State the blood parasite species.
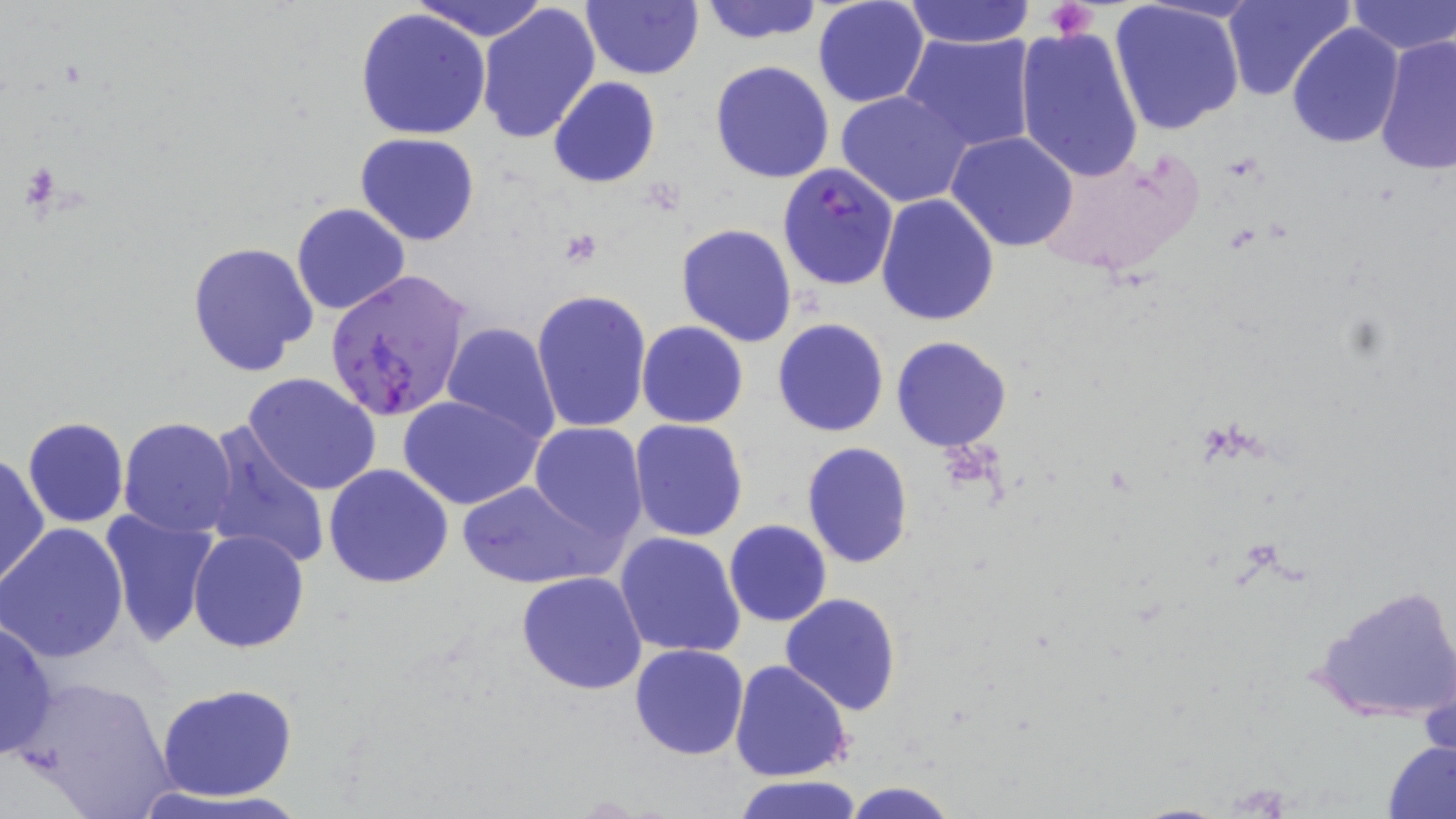
Plasmodium falciparum.

platelet_locations: 'approximate bounding boxes as [x1, y1, x2, y2] in pixels: [1047, 1, 1096, 42], [21, 162, 60, 211]'
magnification: 1000x
field_of_view: single
plasmodium_falciparum_infected_red_blood_cell_locations: 'approximate bounding boxes as [x1, y1, x2, y2] in pixels: [776, 162, 899, 292], [324, 268, 472, 424]'
modality: light microscopy
stain: May-Grünwald-Giemsa
preparation: thin blood smear
uninfected_red_blood_cell_locations: 'approximate bounding boxes as [x1, y1, x2, y2] in pixels: [581, 0, 703, 81], [698, 0, 823, 45], [811, 0, 929, 109], [1224, 0, 1350, 102], [1345, 0, 1456, 56], [413, 1, 551, 42], [902, 1, 1036, 47], [1109, 2, 1244, 138], [477, 4, 601, 144], [356, 6, 491, 141], [1285, 23, 1403, 148], [1014, 27, 1145, 183], [900, 33, 1039, 151], [1374, 34, 1456, 178], [710, 60, 836, 185], [549, 76, 660, 188], [836, 91, 971, 208], [947, 131, 1078, 251], [354, 134, 480, 245], [1030, 146, 1206, 279], [877, 194, 1000, 326], [291, 202, 411, 316], [677, 224, 798, 347], [186, 241, 319, 378], [531, 287, 652, 433], [773, 318, 890, 438], [441, 321, 560, 442], [636, 321, 748, 428], [891, 336, 1011, 453], [241, 373, 383, 496], [399, 393, 546, 511], [22, 417, 130, 528], [117, 417, 238, 538], [627, 418, 749, 541], [529, 420, 650, 539], [202, 424, 331, 572], [801, 442, 915, 569], [1, 453, 49, 592], [324, 463, 454, 589], [457, 478, 615, 590], [97, 510, 219, 651], [724, 519, 832, 626], [0, 524, 129, 665], [188, 529, 309, 653], [615, 531, 745, 660], [516, 571, 648, 695], [1310, 580, 1456, 726], [780, 593, 903, 715], [0, 619, 57, 761], [628, 644, 749, 761], [731, 660, 853, 783], [19, 673, 177, 818], [155, 682, 300, 803], [1382, 737, 1455, 819], [733, 774, 865, 819], [842, 781, 958, 818]'
image_size: 1456×819 pixels